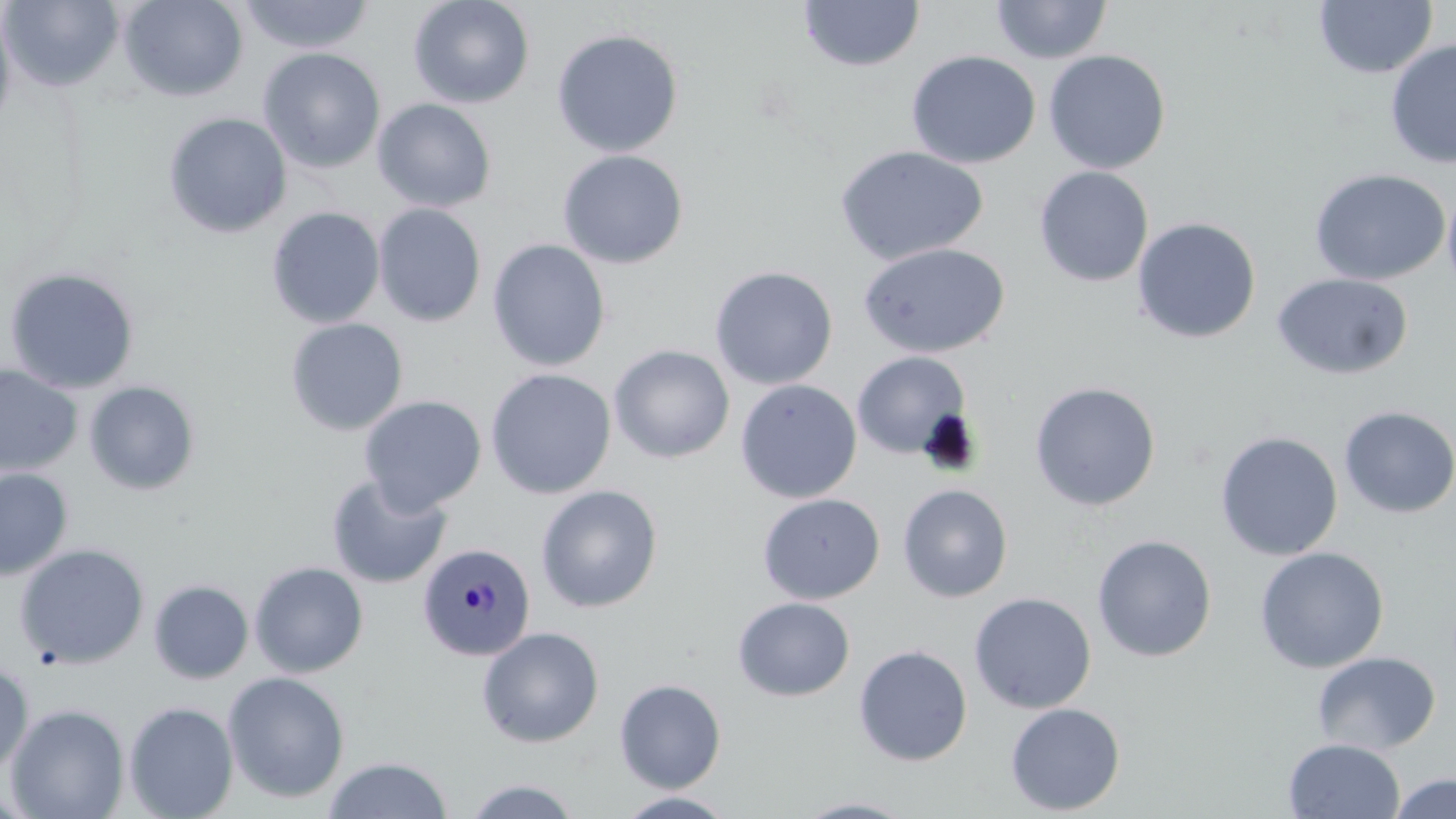

slide-level diagnosis = Plasmodium malariae
preparation = thin blood film
magnification = 1000x
Plasmodium malariae-infected red blood cell locations = approximate bounding boxes as (x1, y1, x2, y2) in pixels: (417, 541, 536, 661)
field of view = one of a larger specimen
uninfected red blood cell locations = approximate bounding boxes as (x1, y1, x2, y2) in pixels: (1, 0, 125, 91), (118, 0, 249, 102), (237, 0, 376, 55), (408, 0, 535, 109), (990, 0, 1112, 64), (798, 1, 924, 72), (1314, 1, 1437, 79), (0, 4, 17, 139), (551, 28, 684, 158), (1385, 38, 1456, 169), (258, 47, 386, 173), (906, 50, 1041, 169), (1043, 50, 1171, 174), (373, 98, 497, 213), (163, 112, 292, 238), (835, 145, 990, 265), (557, 150, 688, 269), (1034, 166, 1153, 287), (1310, 167, 1450, 286), (1442, 182, 1456, 299), (373, 203, 487, 327), (266, 206, 385, 328), (1131, 216, 1262, 344), (487, 239, 611, 372), (857, 242, 1010, 359), (709, 265, 838, 390), (3, 266, 140, 394), (1271, 273, 1413, 380), (285, 317, 408, 436), (609, 345, 735, 463), (851, 351, 972, 460), (0, 364, 82, 477), (485, 368, 616, 499), (735, 379, 862, 503), (83, 380, 201, 496), (1029, 381, 1161, 511), (358, 395, 486, 516), (1338, 406, 1456, 519), (1214, 431, 1343, 561), (0, 468, 73, 581), (326, 475, 452, 589), (897, 483, 1013, 603), (536, 484, 663, 613), (757, 493, 884, 604), (1092, 534, 1217, 662), (14, 543, 150, 669), (1254, 546, 1390, 674), (249, 561, 369, 678), (148, 579, 254, 684), (969, 591, 1097, 714), (732, 597, 855, 701), (476, 626, 605, 748), (853, 644, 973, 767), (1312, 651, 1441, 755), (0, 662, 34, 775), (222, 671, 350, 804), (615, 678, 726, 793), (123, 702, 238, 819), (1005, 702, 1125, 815), (5, 703, 130, 819), (1283, 738, 1406, 819), (323, 756, 453, 818), (1386, 773, 1456, 819), (459, 777, 584, 818), (614, 791, 738, 818), (794, 797, 919, 818)
modality = optical microscopy
stain = May-Grünwald-Giemsa
image size = 1456×819 pixels